Give a bounding box for every artifact (stain precipitate or debris).
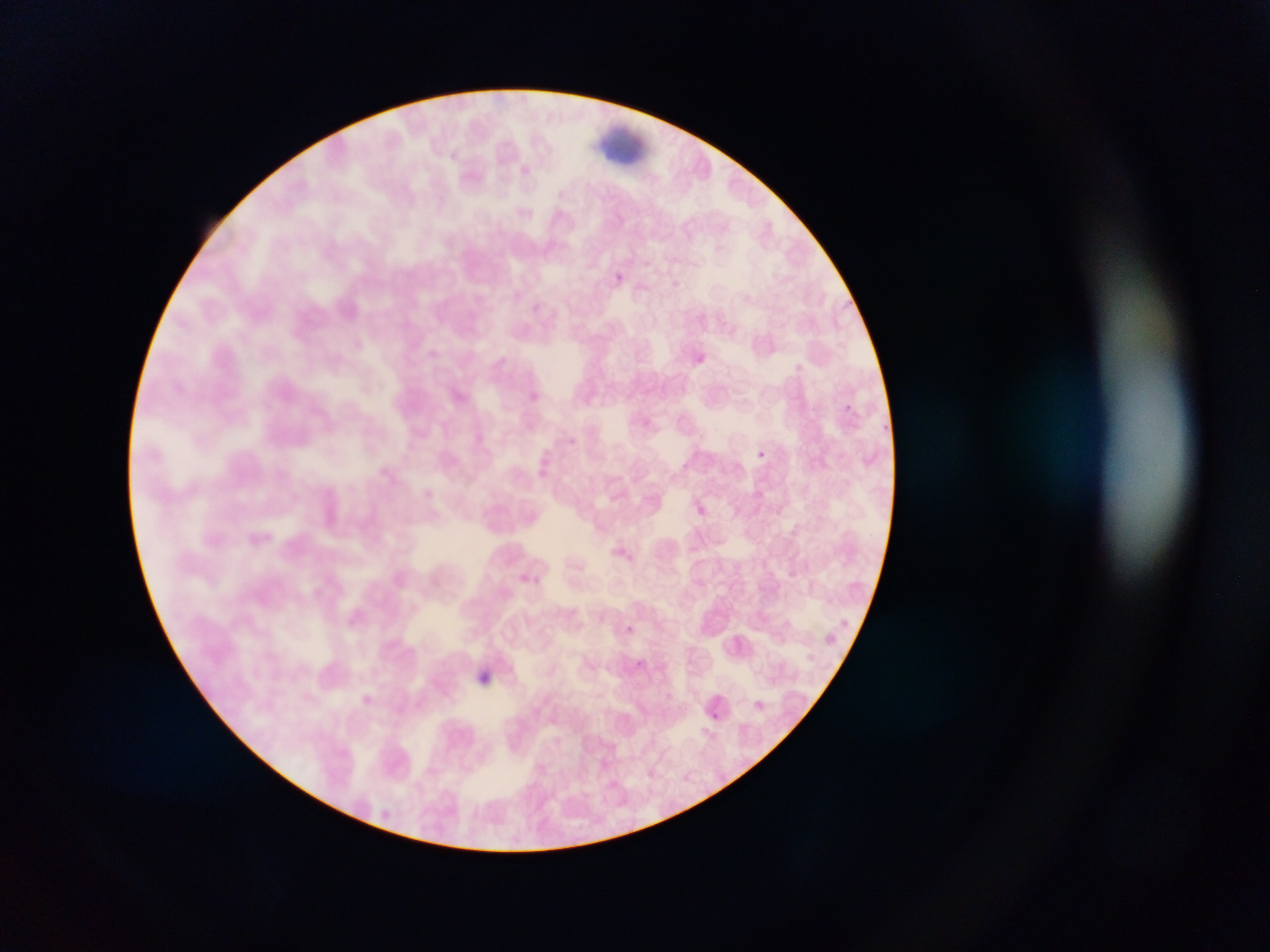

Approximate bounding boxes as left top right bottom in pixels.
Artifacts (stain precipitate or debris): 601 115 643 167.

capture = mobile-phone photograph through a microscope
preparation = thin blood film
field of view = single
image size = 1270×952 pixels
country = Ghana
malaria parasite locations = approximate bounding boxes as left top right bottom in pixels: 608 271 627 287; 841 402 855 415; 756 449 767 459; 694 502 707 517; 620 624 637 638; 634 657 648 670; 477 674 493 696; 352 688 378 713